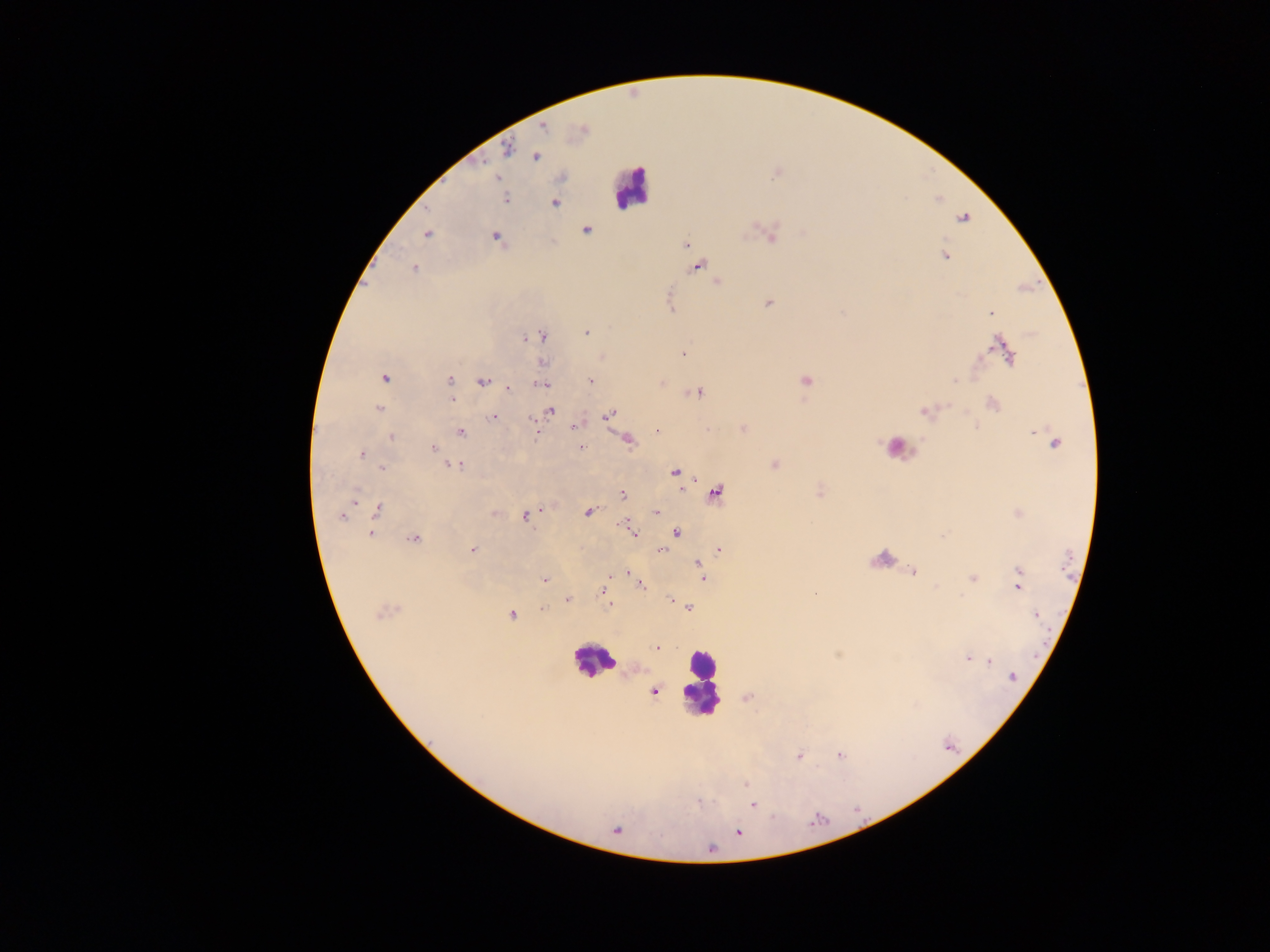

capture = mobile-phone photograph through a microscope
leukocyte locations = approximate centers as {x, y} in pixels: {631, 187}, {896, 448}, {881, 558}, {593, 660}, {702, 682}
Plasmodium parasite locations = approximate centers as {x, y} in pixels: {542, 125}, {582, 130}, {508, 149}, {535, 156}, {505, 199}, {554, 202}, {962, 218}, {585, 230}, {426, 233}, {770, 235}, {496, 238}, {685, 245}, {946, 256}, {697, 265}, {413, 269}, {716, 282}, {768, 304}, {670, 305}, {991, 312}, {586, 332}, {541, 336}, {1001, 348}, {683, 352}, {602, 357}, {542, 363}, {384, 377}, {449, 380}, {591, 380}, {484, 381}, {805, 381}, {661, 383}, {541, 384}, {507, 387}, {696, 391}, {451, 399}, {992, 403}, {379, 409}, {550, 410}, {925, 410}, {610, 413}, {492, 416}, {576, 425}, {743, 428}, {657, 430}, {1034, 431}, {460, 432}, {535, 432}, {392, 437}, {626, 440}, {1054, 443}, {582, 447}, {433, 448}, {361, 454}, {774, 464}, {454, 466}, {382, 468}, {675, 472}, {819, 492}, {714, 493}, {623, 494}, {353, 497}, {377, 510}, {588, 512}, {656, 512}, {1018, 512}, {494, 513}, {343, 515}, {527, 515}, {628, 527}, {633, 532}, {676, 532}, {370, 533}, {414, 539}, {472, 549}, {660, 550}, {718, 550}, {698, 563}, {700, 569}, {625, 572}, {912, 572}, {1018, 572}, {612, 575}, {702, 576}, {972, 577}, {544, 580}, {639, 584}, {1017, 585}, {603, 590}, {815, 593}, {567, 598}, {670, 599}, {609, 605}, {542, 608}, {688, 608}, {385, 611}, {511, 614}, {1035, 614}, {655, 647}, {968, 658}, {987, 660}, {1011, 676}, {653, 691}, {748, 697}, {839, 755}, {798, 756}, {745, 784}, {698, 801}, {752, 804}, {615, 829}, {737, 831}
country = Ghana
image size = 1270×952 pixels
field of view = single
preparation = thick blood film